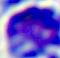
Summary:
  - Modality: photomicrograph
  - Magnification: 400x
  - Identification: white blood cell